Assess this cell for malaria.
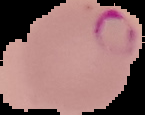

It is parasitized.

Cell region segmented out of the field of view; the surrounding area is masked to black. Image is 145×115 pixels. From a thin blood smear.